Classify this cell by malaria status.
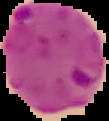

Parasitized.

Summary:
  - Image type: cell region segmented out of the field of view; surrounding area masked to black
  - Preparation: thin blood film
  - Image size: 109×121 pixels